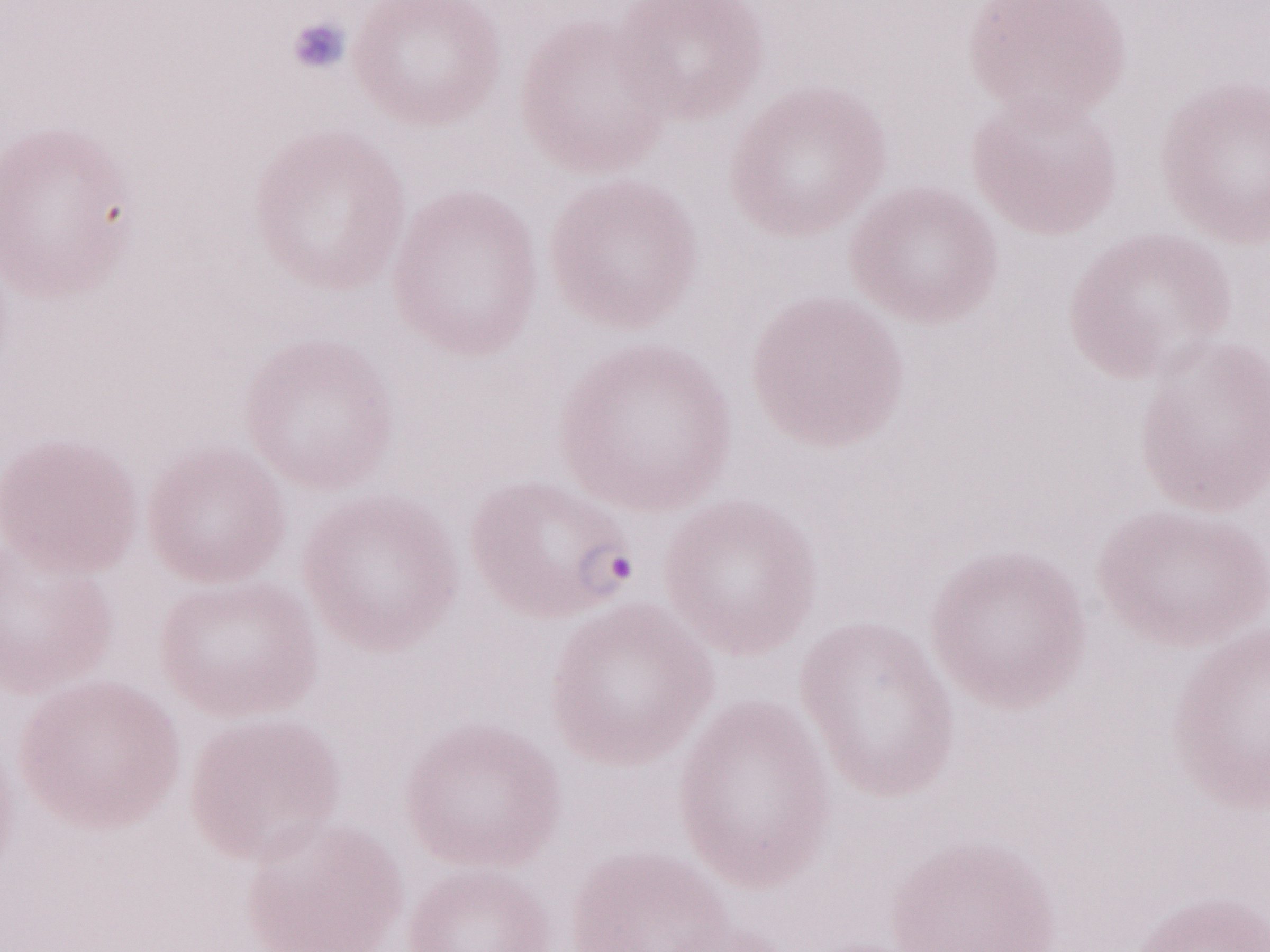
May-Grünwald-Giemsa-stained preparation. One field of this slide. Olympus BX43 microscope, Olympus DP73 camera. Image is 1270×952 pixels. Magnification: 1,000x. Thin blood film. Patient diagnosis: malaria infection.